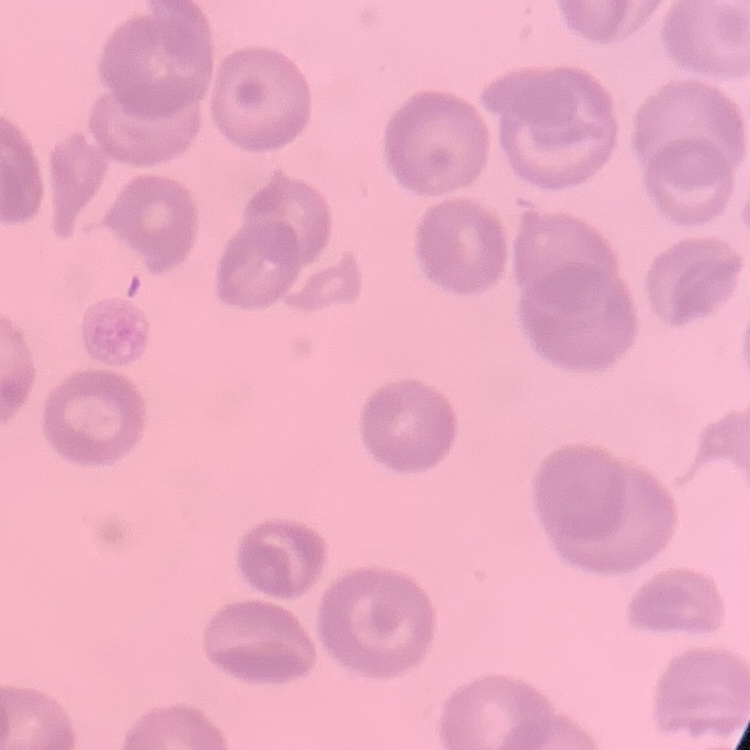
The erythrocytes show no rouleaux formation. Thin peripheral smear. One tile cut from a larger photomicrograph. Field's or Giemsa stain.